Assess this cell for malaria.
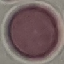
Uninfected.

stain = Giemsa
preparation = thin blood film
capture = smartphone camera at the microscope eyepiece
image type = cell patch, automatically extracted from a larger field of view and resized to 64 × 64 pixels